Locate and identify every blood parasite.
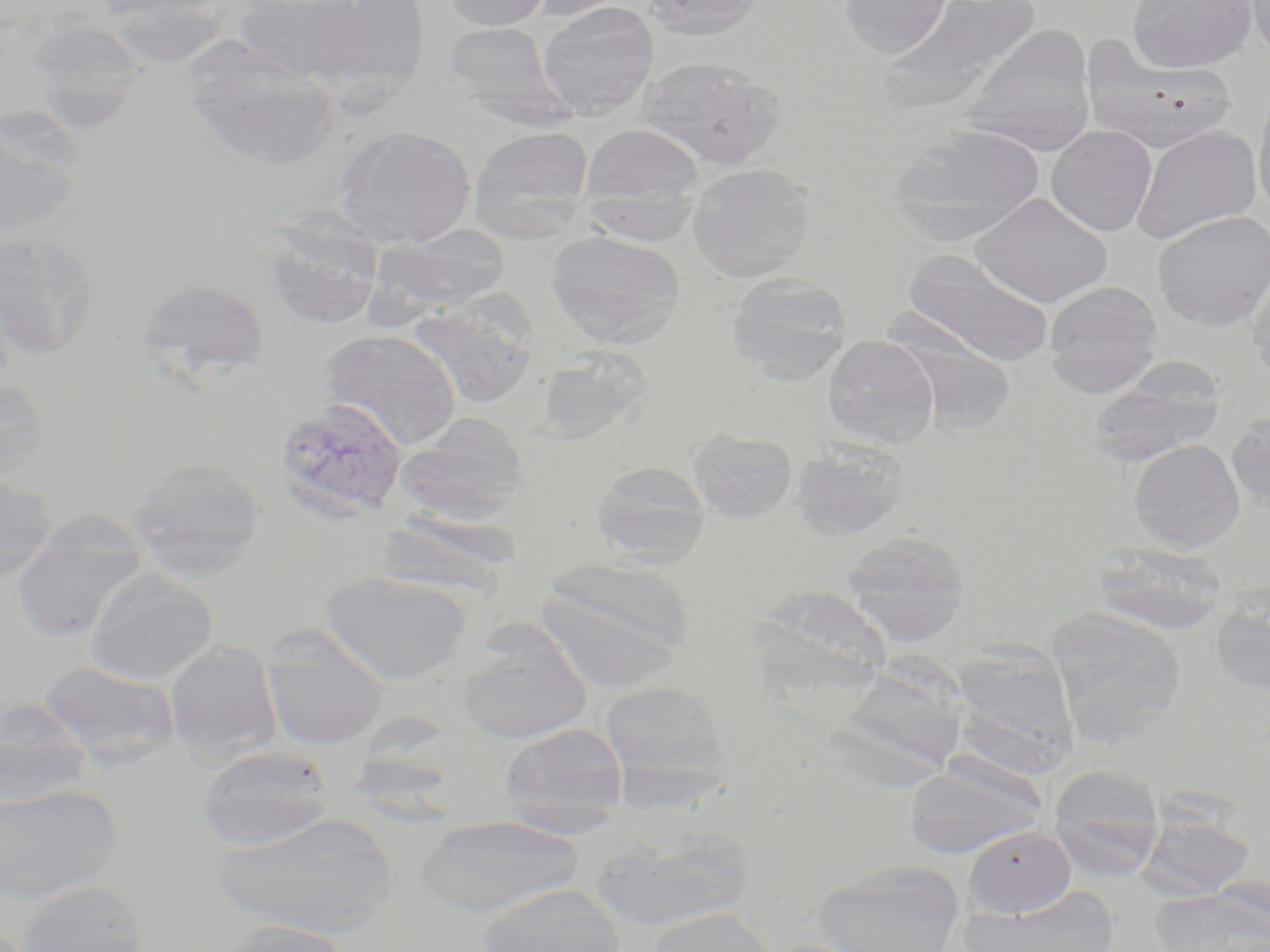
Approximate bounding boxes as named x1/y1/x2/y2 corners in pixels.
Plasmodium vivax-infected red blood cells: (x1=273, y1=397, x2=408, y2=525).
No Plasmodium falciparum, Plasmodium ovale, Plasmodium malariae, Babesia divergens, or Trypanosoma brucei observed.

slide-level diagnosis = Plasmodium vivax
modality = optical microscopy
field of view = one of a larger specimen
preparation = thin blood film
magnification = 1000x
uninfected red blood cell locations = approximate bounding boxes as named x1/y1/x2/y2 corners in pixels: (x1=234, y1=0, x2=371, y2=84), (x1=318, y1=0, x2=432, y2=100), (x1=442, y1=0, x2=553, y2=31), (x1=526, y1=0, x2=640, y2=21), (x1=640, y1=0, x2=764, y2=40), (x1=838, y1=0, x2=951, y2=57), (x1=1128, y1=0, x2=1257, y2=73), (x1=1246, y1=0, x2=1270, y2=65), (x1=875, y1=1, x2=1045, y2=118), (x1=537, y1=2, x2=659, y2=118), (x1=30, y1=16, x2=145, y2=132), (x1=443, y1=22, x2=566, y2=118), (x1=961, y1=24, x2=1097, y2=157), (x1=183, y1=36, x2=340, y2=171), (x1=1081, y1=37, x2=1237, y2=153), (x1=638, y1=56, x2=786, y2=171), (x1=1253, y1=88, x2=1270, y2=218), (x1=0, y1=110, x2=85, y2=240), (x1=579, y1=123, x2=703, y2=225), (x1=335, y1=125, x2=476, y2=248), (x1=890, y1=125, x2=1046, y2=245), (x1=1046, y1=125, x2=1157, y2=237), (x1=469, y1=126, x2=594, y2=243), (x1=1131, y1=126, x2=1263, y2=245), (x1=687, y1=163, x2=815, y2=281), (x1=972, y1=193, x2=1113, y2=308), (x1=1153, y1=211, x2=1270, y2=331), (x1=264, y1=213, x2=385, y2=331), (x1=368, y1=225, x2=510, y2=318), (x1=0, y1=230, x2=101, y2=361), (x1=545, y1=231, x2=685, y2=349), (x1=902, y1=249, x2=1055, y2=368), (x1=1248, y1=256, x2=1270, y2=384), (x1=727, y1=273, x2=853, y2=385), (x1=138, y1=277, x2=271, y2=382), (x1=1044, y1=281, x2=1163, y2=397), (x1=409, y1=299, x2=538, y2=409), (x1=318, y1=329, x2=460, y2=450), (x1=895, y1=333, x2=1018, y2=433), (x1=823, y1=335, x2=938, y2=448), (x1=536, y1=346, x2=655, y2=444), (x1=1087, y1=361, x2=1227, y2=469), (x1=0, y1=378, x2=51, y2=484), (x1=396, y1=411, x2=531, y2=521), (x1=1226, y1=411, x2=1270, y2=511), (x1=688, y1=427, x2=797, y2=523), (x1=1129, y1=439, x2=1245, y2=552), (x1=791, y1=440, x2=908, y2=541), (x1=127, y1=455, x2=267, y2=578), (x1=590, y1=460, x2=712, y2=566), (x1=0, y1=472, x2=57, y2=584), (x1=375, y1=510, x2=524, y2=595), (x1=12, y1=513, x2=149, y2=642), (x1=841, y1=532, x2=970, y2=645), (x1=1093, y1=543, x2=1226, y2=635), (x1=537, y1=556, x2=695, y2=681), (x1=85, y1=568, x2=219, y2=683), (x1=321, y1=570, x2=470, y2=684), (x1=748, y1=583, x2=893, y2=694), (x1=1208, y1=597, x2=1270, y2=697), (x1=1045, y1=610, x2=1187, y2=744), (x1=260, y1=627, x2=390, y2=750), (x1=457, y1=636, x2=591, y2=744), (x1=165, y1=640, x2=282, y2=764), (x1=948, y1=644, x2=1079, y2=773), (x1=38, y1=660, x2=179, y2=770), (x1=825, y1=661, x2=968, y2=783), (x1=599, y1=678, x2=732, y2=800), (x1=0, y1=696, x2=93, y2=805), (x1=498, y1=722, x2=630, y2=833), (x1=197, y1=745, x2=336, y2=850), (x1=902, y1=756, x2=1049, y2=859), (x1=1048, y1=764, x2=1164, y2=880), (x1=0, y1=784, x2=121, y2=904), (x1=211, y1=811, x2=398, y2=937), (x1=1137, y1=811, x2=1256, y2=901), (x1=412, y1=815, x2=584, y2=917), (x1=591, y1=826, x2=755, y2=932), (x1=963, y1=827, x2=1076, y2=917), (x1=812, y1=860, x2=964, y2=952), (x1=16, y1=879, x2=147, y2=952), (x1=1150, y1=882, x2=1270, y2=952), (x1=476, y1=884, x2=628, y2=952), (x1=963, y1=885, x2=1121, y2=952), (x1=646, y1=906, x2=775, y2=952), (x1=214, y1=920, x2=356, y2=952)
stain = May-Grünwald-Giemsa
image size = 1270×952 pixels